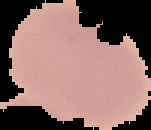
image type = segmented cell region on a black background
image size = 151×130 pixels
malaria status = uninfected
preparation = thin blood smear